Classify this cell by malaria status.
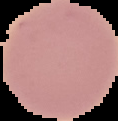
It is uninfected.

preparation = thin blood smear
image size = 118×121 pixels
image type = segmented cell region on a black background